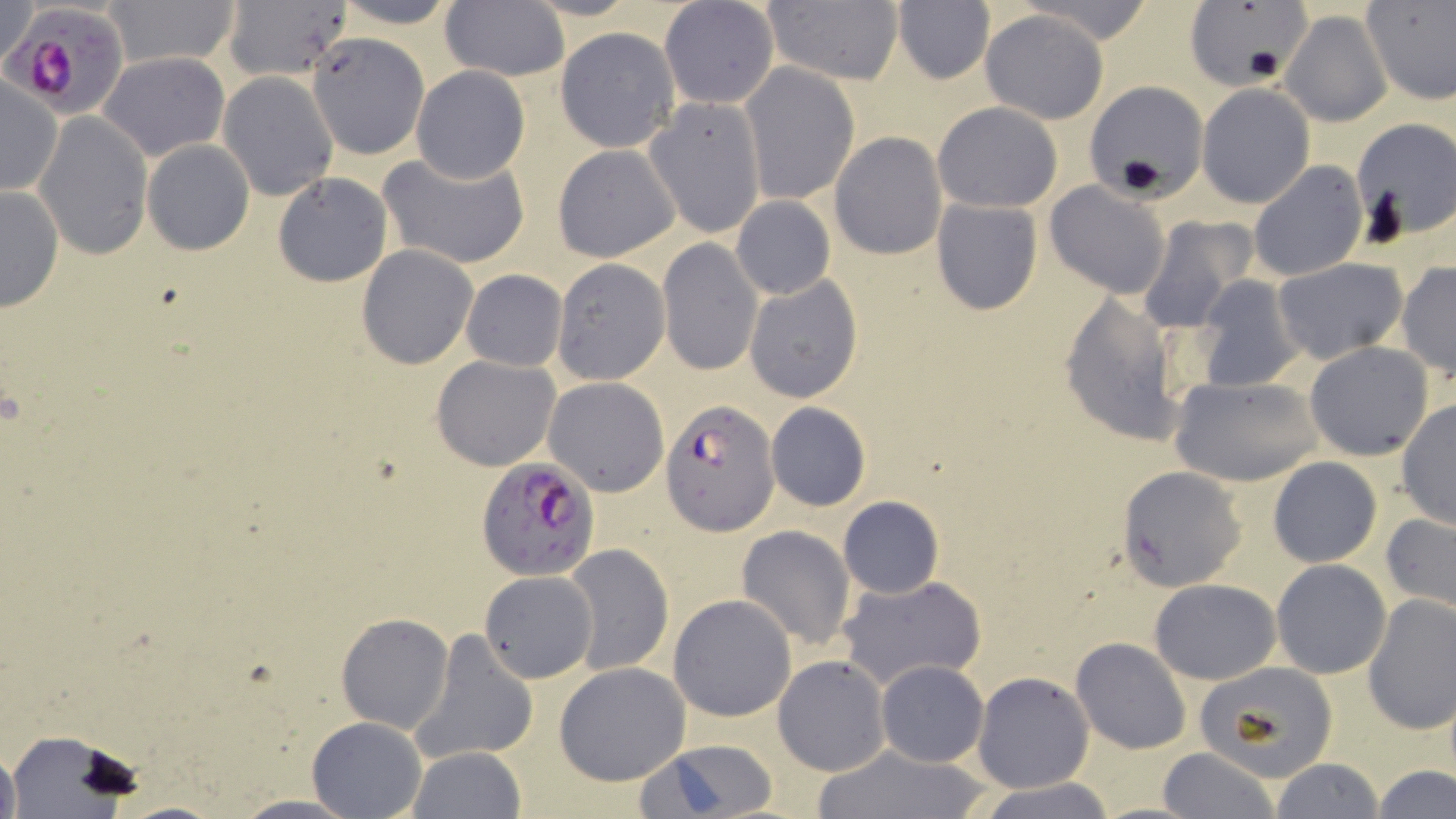

plasmodium_falciparum_infected_red_blood_cell_locations: 'approximate bounding boxes as named x1/y1/x2/y2 corners in pixels: (x1=3, y1=0, x2=137, y2=117), (x1=660, y1=398, x2=778, y2=536), (x1=475, y1=453, x2=602, y2=580)'
slide_level_diagnosis: Plasmodium falciparum
magnification: 1000x
preparation: thin blood film
stain: May-Grünwald-Giemsa
field_of_view: one of a larger specimen
image_size: 1456×819 pixels
modality: light microscopy
uninfected_red_blood_cell_locations: 'approximate bounding boxes as named x1/y1/x2/y2 corners in pixels: (x1=1, y1=0, x2=41, y2=71), (x1=104, y1=0, x2=239, y2=68), (x1=220, y1=0, x2=351, y2=84), (x1=330, y1=0, x2=467, y2=29), (x1=438, y1=1, x2=569, y2=82), (x1=659, y1=1, x2=780, y2=110), (x1=759, y1=1, x2=904, y2=86), (x1=891, y1=1, x2=995, y2=86), (x1=1362, y1=1, x2=1456, y2=106), (x1=1184, y1=3, x2=1305, y2=90), (x1=980, y1=10, x2=1109, y2=123), (x1=1279, y1=11, x2=1391, y2=127), (x1=555, y1=28, x2=679, y2=152), (x1=309, y1=33, x2=433, y2=156), (x1=98, y1=51, x2=229, y2=160), (x1=740, y1=62, x2=860, y2=206), (x1=410, y1=66, x2=530, y2=183), (x1=217, y1=72, x2=339, y2=200), (x1=1, y1=76, x2=61, y2=196), (x1=1086, y1=81, x2=1208, y2=194), (x1=1196, y1=83, x2=1316, y2=209), (x1=643, y1=97, x2=766, y2=237), (x1=933, y1=102, x2=1062, y2=212), (x1=34, y1=112, x2=153, y2=260), (x1=1349, y1=117, x2=1456, y2=242), (x1=831, y1=132, x2=946, y2=259), (x1=141, y1=138, x2=256, y2=255), (x1=552, y1=143, x2=680, y2=261), (x1=380, y1=151, x2=531, y2=271), (x1=1247, y1=159, x2=1367, y2=282), (x1=273, y1=172, x2=393, y2=286), (x1=1045, y1=180, x2=1172, y2=300), (x1=0, y1=183, x2=63, y2=313), (x1=730, y1=196, x2=835, y2=300), (x1=934, y1=198, x2=1044, y2=314), (x1=1137, y1=218, x2=1256, y2=333), (x1=657, y1=238, x2=763, y2=376), (x1=357, y1=245, x2=479, y2=368), (x1=1272, y1=257, x2=1408, y2=362), (x1=551, y1=259, x2=669, y2=386), (x1=1396, y1=263, x2=1455, y2=381), (x1=461, y1=269, x2=567, y2=371), (x1=744, y1=273, x2=863, y2=404), (x1=1193, y1=275, x2=1304, y2=392), (x1=1058, y1=292, x2=1187, y2=448), (x1=1304, y1=342, x2=1435, y2=461), (x1=432, y1=355, x2=560, y2=471), (x1=1171, y1=375, x2=1322, y2=486), (x1=542, y1=378, x2=671, y2=497), (x1=1395, y1=399, x2=1455, y2=530), (x1=765, y1=401, x2=872, y2=511), (x1=1268, y1=457, x2=1381, y2=567), (x1=1118, y1=466, x2=1248, y2=591), (x1=837, y1=495, x2=944, y2=599), (x1=1380, y1=512, x2=1456, y2=618), (x1=735, y1=526, x2=855, y2=651), (x1=562, y1=542, x2=674, y2=676), (x1=1271, y1=559, x2=1392, y2=679), (x1=480, y1=569, x2=600, y2=683), (x1=837, y1=573, x2=988, y2=691), (x1=1150, y1=578, x2=1281, y2=684), (x1=667, y1=593, x2=797, y2=722), (x1=1361, y1=594, x2=1456, y2=738), (x1=335, y1=611, x2=454, y2=734), (x1=412, y1=630, x2=537, y2=764), (x1=1070, y1=637, x2=1192, y2=755), (x1=773, y1=655, x2=890, y2=776), (x1=876, y1=660, x2=987, y2=767), (x1=553, y1=661, x2=692, y2=786), (x1=1193, y1=661, x2=1339, y2=781), (x1=972, y1=672, x2=1092, y2=792), (x1=306, y1=716, x2=427, y2=819), (x1=8, y1=731, x2=140, y2=815), (x1=641, y1=738, x2=783, y2=817), (x1=0, y1=741, x2=20, y2=819), (x1=811, y1=743, x2=991, y2=818), (x1=406, y1=747, x2=525, y2=818), (x1=1158, y1=747, x2=1280, y2=819), (x1=1270, y1=757, x2=1385, y2=819), (x1=1373, y1=764, x2=1455, y2=819), (x1=977, y1=780, x2=1118, y2=819), (x1=225, y1=795, x2=366, y2=817)'